Report the malaria status of this cell.
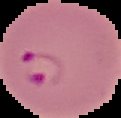

Parasitized.

Image is 121×118 pixels. From a thin blood smear. Segmented cell region on a black background.